Locate every blood parasite and identify its species.
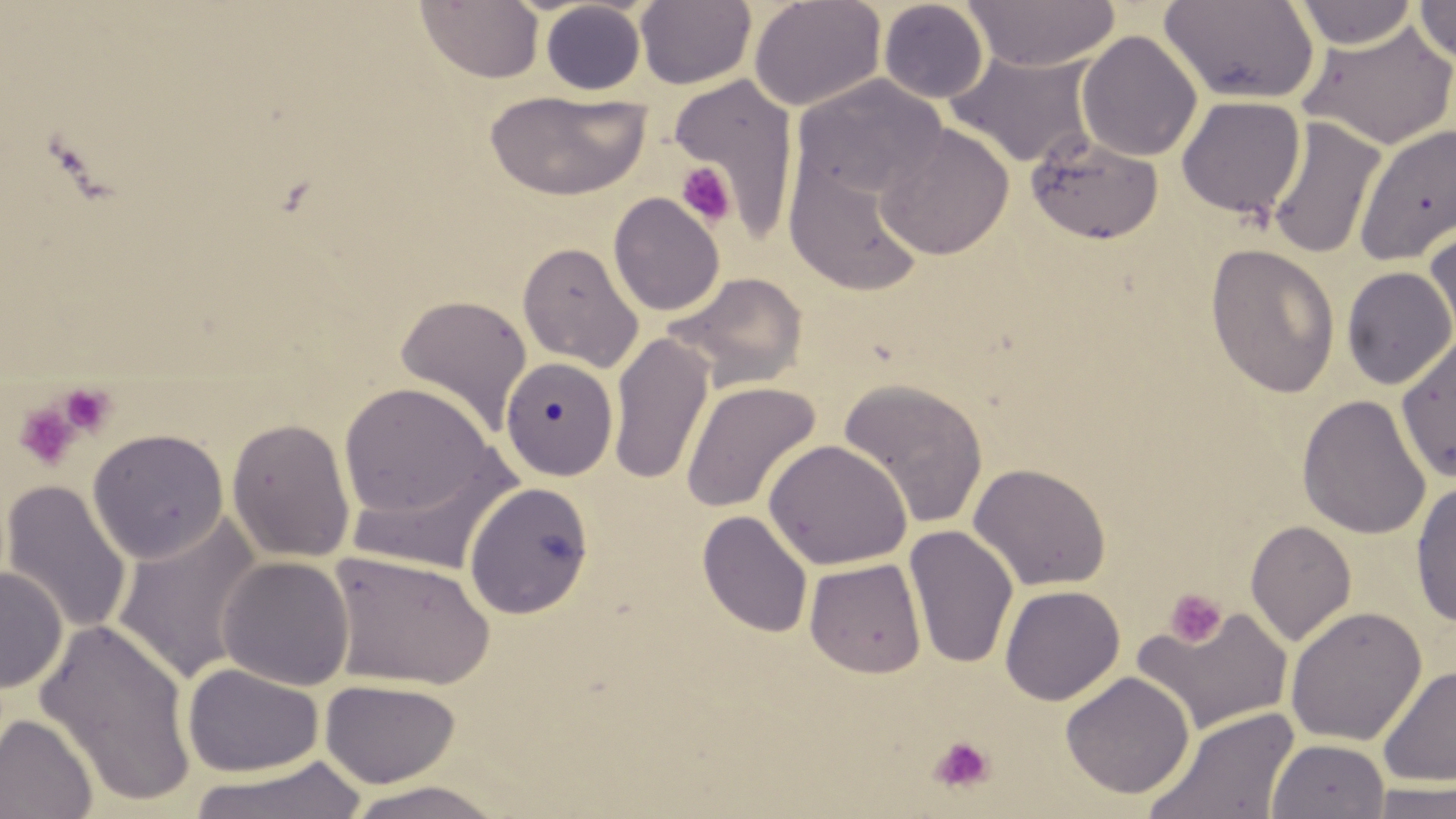

No blood parasites observed.

Summary:
  - Coordinate format: approximate bounding boxes as named x1/y1/x2/y2 corners in pixels
  - Uninfected red blood cell locations: (x1=748, y1=0, x2=886, y2=112), (x1=878, y1=0, x2=990, y2=103), (x1=963, y1=0, x2=1121, y2=71), (x1=1414, y1=0, x2=1456, y2=67), (x1=415, y1=1, x2=544, y2=84), (x1=635, y1=1, x2=757, y2=89), (x1=1159, y1=1, x2=1320, y2=105), (x1=1292, y1=1, x2=1420, y2=49), (x1=540, y1=2, x2=646, y2=95), (x1=1298, y1=18, x2=1456, y2=150), (x1=1077, y1=31, x2=1202, y2=162), (x1=944, y1=47, x2=1100, y2=169), (x1=668, y1=72, x2=800, y2=237), (x1=792, y1=75, x2=948, y2=202), (x1=484, y1=88, x2=650, y2=202), (x1=1176, y1=96, x2=1305, y2=219), (x1=1264, y1=117, x2=1386, y2=260), (x1=875, y1=122, x2=1015, y2=260), (x1=1354, y1=124, x2=1456, y2=267), (x1=1025, y1=134, x2=1164, y2=245), (x1=782, y1=150, x2=927, y2=298), (x1=608, y1=193, x2=725, y2=316), (x1=1424, y1=224, x2=1456, y2=351), (x1=517, y1=241, x2=644, y2=372), (x1=1205, y1=243, x2=1342, y2=399), (x1=1340, y1=267, x2=1456, y2=390), (x1=665, y1=271, x2=808, y2=392), (x1=394, y1=293, x2=532, y2=435), (x1=608, y1=332, x2=714, y2=487), (x1=1396, y1=333, x2=1456, y2=483), (x1=501, y1=356, x2=621, y2=481), (x1=837, y1=377, x2=989, y2=531), (x1=680, y1=380, x2=821, y2=516), (x1=339, y1=382, x2=503, y2=529), (x1=1296, y1=394, x2=1432, y2=540), (x1=227, y1=416, x2=355, y2=563), (x1=88, y1=428, x2=229, y2=564), (x1=763, y1=439, x2=912, y2=571), (x1=342, y1=443, x2=522, y2=577), (x1=968, y1=462, x2=1112, y2=592), (x1=1410, y1=479, x2=1456, y2=627), (x1=1, y1=480, x2=132, y2=636), (x1=463, y1=481, x2=595, y2=619), (x1=697, y1=510, x2=813, y2=638), (x1=112, y1=515, x2=262, y2=684), (x1=1244, y1=519, x2=1357, y2=646), (x1=903, y1=524, x2=1018, y2=670), (x1=325, y1=551, x2=496, y2=691), (x1=217, y1=556, x2=355, y2=691), (x1=804, y1=558, x2=927, y2=678), (x1=0, y1=566, x2=67, y2=695), (x1=999, y1=585, x2=1125, y2=706), (x1=1133, y1=605, x2=1294, y2=736), (x1=1284, y1=606, x2=1427, y2=746), (x1=35, y1=617, x2=198, y2=809), (x1=182, y1=662, x2=323, y2=777), (x1=1377, y1=664, x2=1456, y2=788), (x1=1060, y1=671, x2=1195, y2=799), (x1=319, y1=678, x2=460, y2=788), (x1=1141, y1=707, x2=1302, y2=819), (x1=0, y1=712, x2=98, y2=819), (x1=1267, y1=738, x2=1390, y2=819), (x1=188, y1=756, x2=369, y2=819), (x1=343, y1=779, x2=511, y2=818), (x1=1364, y1=780, x2=1456, y2=819)
  - Platelet locations: (x1=676, y1=162, x2=736, y2=227), (x1=57, y1=382, x2=118, y2=437), (x1=13, y1=401, x2=83, y2=472), (x1=1164, y1=588, x2=1227, y2=648), (x1=928, y1=735, x2=996, y2=794)
  - Slide-level diagnosis: no evidence of blood parasites
  - Modality: optical microscopy
  - Preparation: thin blood smear
  - Field of view: single
  - Image size: 1456×819 pixels
  - Magnification: 1000x
  - Stain: May-Grünwald-Giemsa